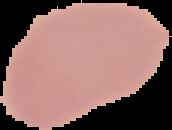
image type = cell region segmented out of the field of view; surrounding area masked to black
image size = 172×130 pixels
preparation = thin blood film
result = negative for malaria parasites